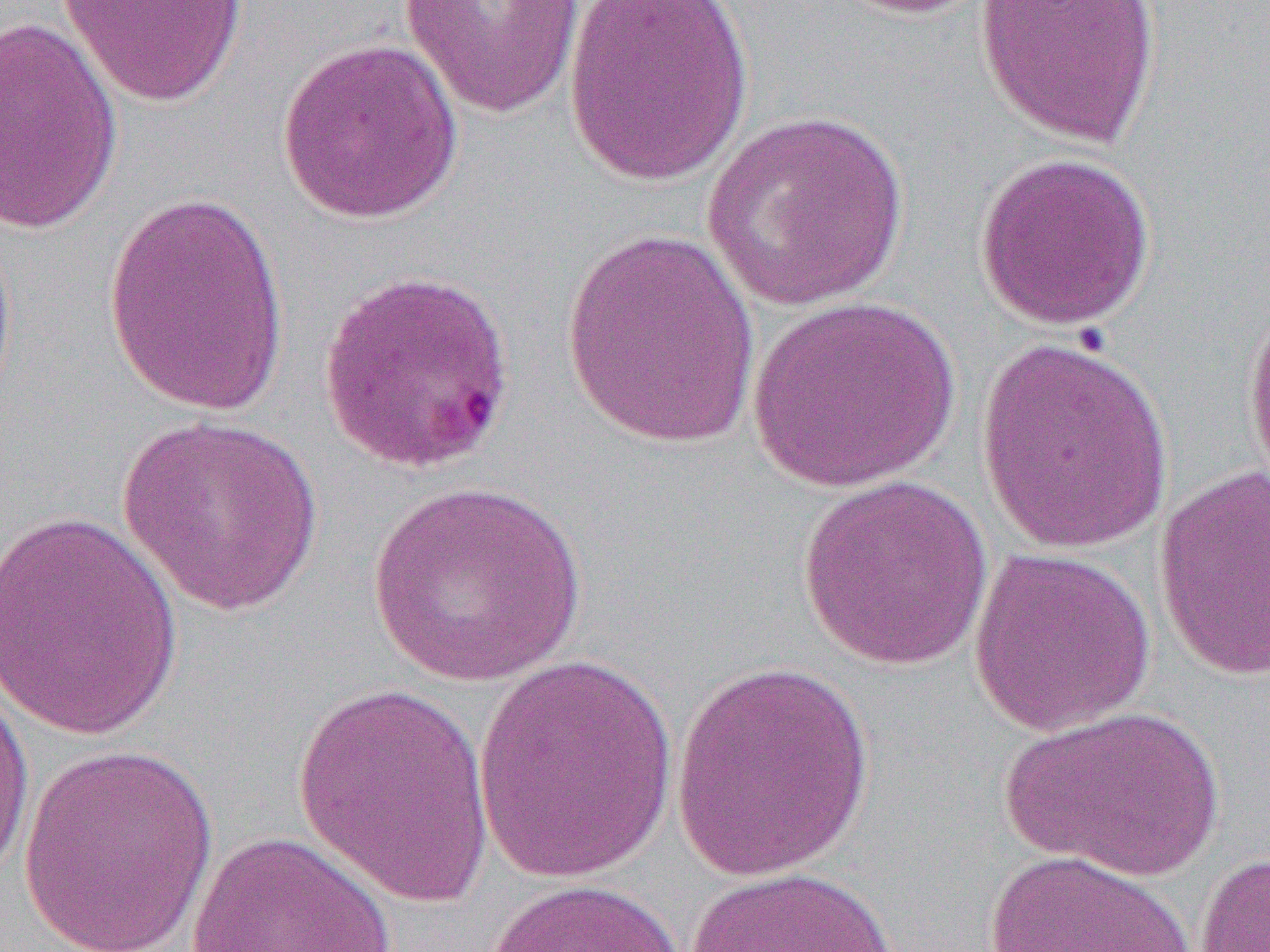
slide-level diagnosis = Plasmodium falciparum
modality = light microscopy
uninfected red blood cell locations = approximate bounding boxes as [x1, y1, x2, y2] in pixels: [55, 0, 249, 109], [398, 0, 587, 120], [564, 0, 755, 186], [825, 0, 998, 19], [974, 0, 1163, 148], [0, 17, 124, 235], [276, 38, 464, 226], [700, 111, 912, 313], [972, 150, 1157, 331], [101, 188, 294, 417], [0, 226, 18, 421], [557, 227, 762, 448], [315, 268, 519, 476], [747, 295, 960, 491], [1241, 297, 1270, 497], [976, 334, 1174, 556], [117, 414, 324, 617], [1154, 466, 1269, 683], [797, 476, 993, 672], [367, 480, 588, 687], [0, 508, 185, 744], [968, 546, 1157, 737], [471, 654, 680, 883], [670, 661, 876, 881], [0, 679, 36, 891], [292, 682, 497, 908], [1001, 705, 1224, 880], [17, 745, 220, 952], [183, 829, 400, 952], [979, 849, 1206, 952], [1195, 851, 1270, 951], [683, 866, 902, 952], [483, 876, 684, 952]
magnification = 1000x
field of view = single
image size = 1270×952 pixels
preparation = thin blood smear